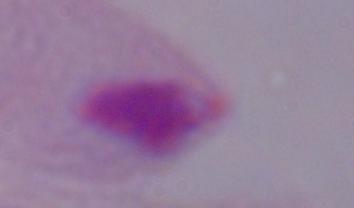

magnification = 1000x
modality = micrograph
identification = trichomonad